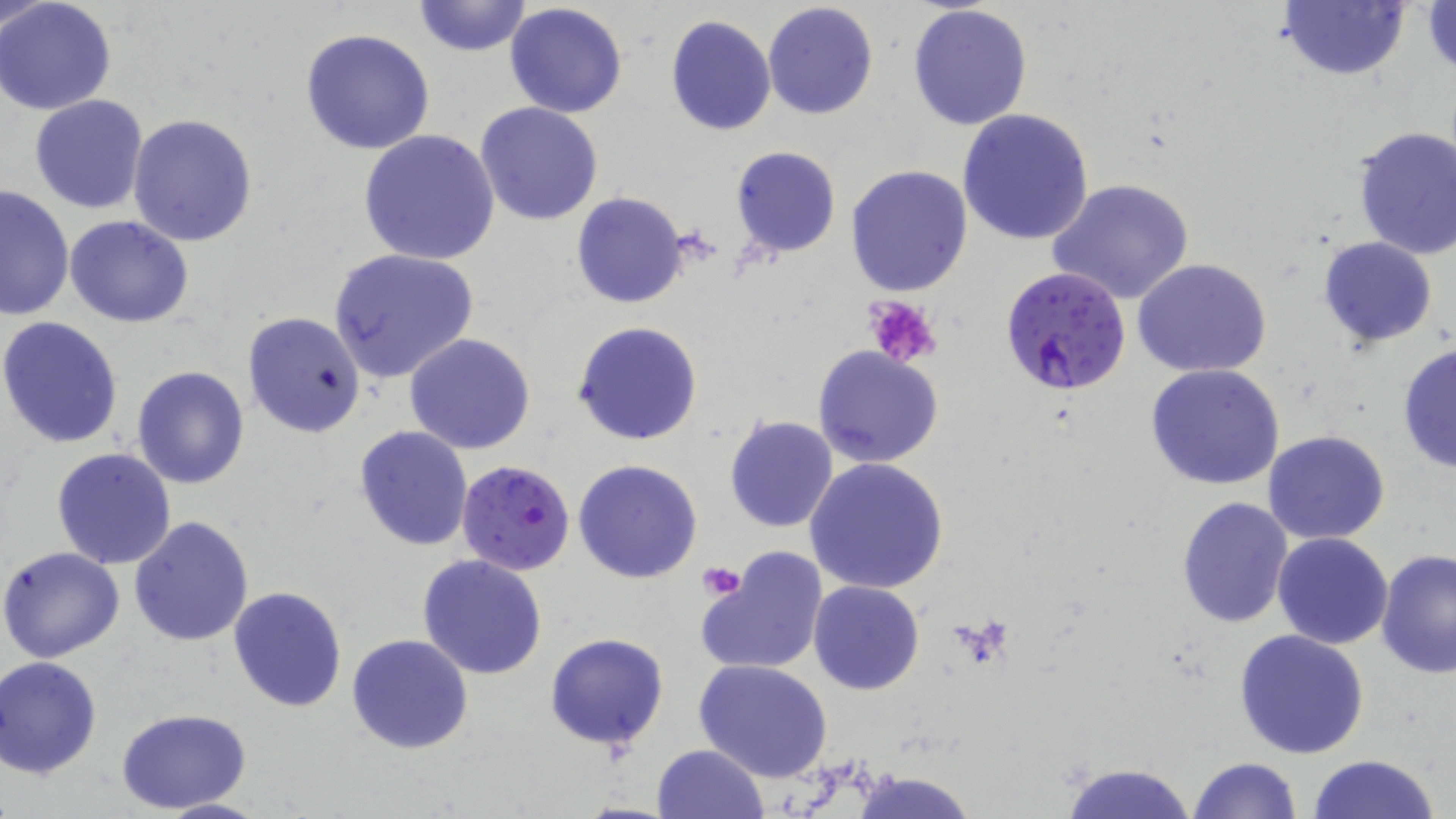 Approximate bounding boxes as (x1, y1, x2, y2) in pixels. Uninfected red blood cell locations: (1, 0, 53, 40), (0, 1, 119, 115), (412, 1, 531, 57), (504, 1, 629, 118), (762, 1, 879, 120), (1278, 1, 1410, 80), (1423, 1, 1455, 79), (907, 4, 1033, 131), (663, 15, 776, 136), (299, 28, 438, 155), (28, 95, 148, 213), (475, 102, 604, 225), (956, 109, 1095, 247), (127, 113, 258, 246), (1351, 125, 1456, 260), (357, 130, 500, 265), (731, 145, 841, 259), (844, 165, 973, 298), (1047, 178, 1194, 306), (0, 183, 73, 322), (571, 192, 689, 309), (66, 215, 194, 327), (1317, 235, 1437, 347), (328, 247, 479, 383), (1131, 257, 1272, 378), (242, 310, 366, 437), (0, 317, 124, 449), (573, 320, 703, 446), (404, 334, 536, 455), (1397, 341, 1456, 474), (813, 345, 944, 468), (1144, 363, 1286, 490), (132, 366, 250, 488), (723, 415, 839, 533), (354, 425, 473, 550), (1264, 430, 1391, 545), (51, 447, 178, 569), (804, 456, 951, 595), (573, 458, 703, 583), (1175, 496, 1292, 629), (129, 516, 254, 647), (1272, 531, 1394, 649), (0, 546, 126, 663), (696, 547, 830, 678), (1376, 550, 1456, 680), (417, 555, 548, 679), (809, 580, 925, 694), (227, 586, 348, 713), (1235, 629, 1371, 759), (543, 632, 669, 751), (347, 633, 473, 753), (0, 656, 103, 779), (694, 659, 833, 782), (115, 707, 255, 814), (651, 744, 769, 819), (1307, 753, 1444, 819), (1188, 757, 1304, 818), (1058, 762, 1199, 819), (154, 797, 269, 818). Plasmodium falciparum-infected red blood cell locations: (999, 265, 1133, 396), (457, 458, 575, 574). Platelet locations: (863, 296, 940, 367), (698, 562, 747, 600). Slide-level diagnosis: Plasmodium falciparum. Thin blood film. One field of a larger specimen. Captured at 1000x magnification. Light microscopy. Image is 1456×819 pixels. May-Grünwald-Giemsa stain.